Outline each uninfected red blood cell.
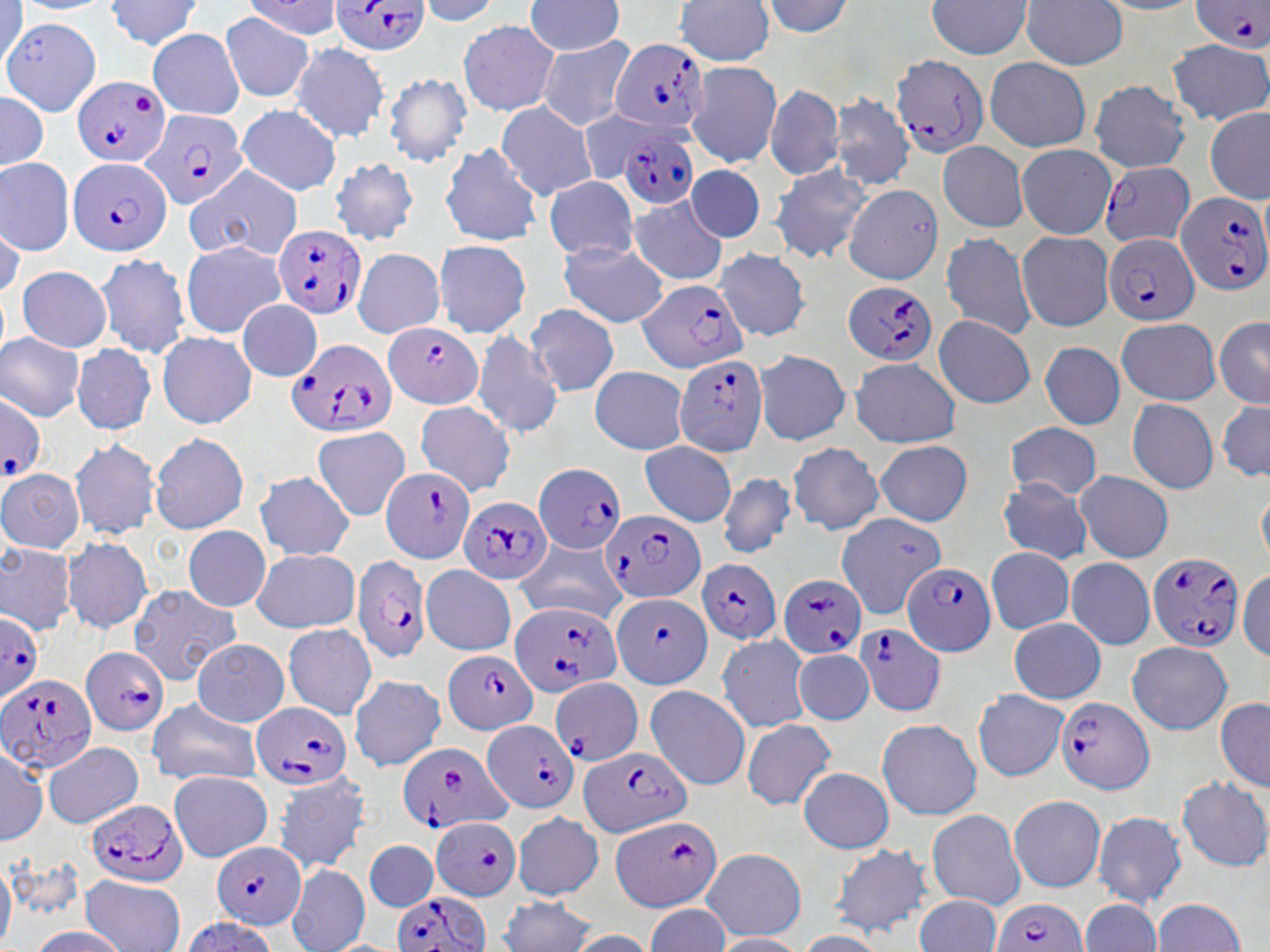
Approximate bounding boxes as [x1, y1, x2, y2] in pixels.
Uninfected red blood cells: [104, 0, 198, 51], [526, 0, 622, 52], [673, 0, 774, 66], [923, 0, 1034, 52], [1011, 0, 1128, 66], [768, 2, 857, 43], [3, 12, 100, 116], [223, 12, 313, 98], [461, 23, 557, 113], [147, 30, 245, 123], [541, 38, 633, 132], [1169, 42, 1270, 122], [289, 45, 389, 144], [986, 58, 1087, 154], [697, 64, 780, 164], [385, 71, 471, 165], [768, 89, 840, 179], [835, 91, 911, 189], [1093, 95, 1189, 169], [985, 96, 1089, 151], [500, 102, 595, 201], [1204, 102, 1268, 206], [238, 106, 340, 196], [685, 129, 774, 166], [444, 144, 539, 245], [937, 145, 1026, 229], [1019, 145, 1109, 240], [1, 156, 72, 256], [333, 163, 419, 245], [773, 163, 868, 263], [688, 168, 761, 240], [546, 178, 634, 256], [845, 181, 943, 287], [185, 183, 301, 261], [629, 197, 727, 284], [1021, 234, 1111, 330], [945, 235, 1034, 337], [561, 240, 670, 327], [185, 244, 283, 335], [439, 244, 527, 336], [722, 249, 811, 339], [99, 252, 188, 359], [355, 252, 441, 336], [21, 268, 110, 352], [242, 301, 318, 378], [527, 306, 617, 396], [1216, 315, 1270, 407], [934, 316, 1032, 407], [1114, 321, 1221, 409], [1, 332, 78, 423], [477, 332, 562, 438], [161, 333, 260, 428], [76, 345, 154, 435], [1040, 345, 1124, 429], [758, 352, 848, 444], [851, 363, 959, 446], [594, 369, 687, 453], [1213, 392, 1270, 485], [1127, 399, 1217, 495], [417, 403, 513, 490], [1010, 423, 1097, 502], [148, 428, 249, 536], [312, 429, 405, 518], [73, 440, 158, 537], [878, 443, 967, 527], [641, 444, 734, 524], [791, 445, 881, 535], [1078, 471, 1173, 560], [255, 473, 356, 560], [0, 475, 86, 554], [1000, 475, 1093, 562], [721, 477, 793, 556], [837, 514, 930, 612], [183, 526, 269, 610], [67, 538, 151, 632], [0, 542, 76, 637], [518, 545, 625, 622], [992, 548, 1071, 634], [249, 551, 357, 631], [1068, 560, 1153, 647], [424, 565, 514, 655], [131, 589, 241, 683], [1010, 620, 1102, 706], [286, 625, 374, 717], [719, 635, 807, 730], [1124, 638, 1232, 735], [194, 641, 288, 727], [798, 652, 873, 724], [354, 677, 441, 772], [648, 686, 750, 788], [975, 689, 1069, 779], [1212, 691, 1268, 789], [150, 704, 262, 786], [745, 719, 834, 812], [878, 719, 980, 817], [4, 737, 46, 852], [45, 744, 142, 831], [797, 766, 893, 854], [170, 775, 270, 861], [1179, 776, 1250, 869], [275, 777, 370, 871], [1009, 792, 1105, 893], [509, 807, 600, 902], [926, 811, 1028, 909], [1096, 815, 1185, 909], [367, 843, 436, 912], [828, 844, 930, 940], [706, 854, 800, 939], [291, 868, 368, 952], [79, 876, 184, 952], [916, 897, 998, 952], [500, 898, 593, 952], [1155, 900, 1245, 952], [1081, 901, 1160, 952].

Summary:
  - Plasmodium falciparum-infected red blood cell locations: [321, 0, 435, 57], [1188, 1, 1270, 52], [611, 38, 708, 133], [891, 50, 989, 162], [72, 74, 170, 167], [142, 112, 248, 211], [622, 136, 697, 207], [1101, 156, 1195, 250], [66, 157, 175, 254], [1173, 194, 1270, 297], [275, 228, 364, 317], [1105, 230, 1199, 325], [837, 279, 942, 365], [639, 285, 745, 376], [381, 321, 484, 410], [287, 338, 393, 436], [672, 348, 771, 456], [1, 398, 41, 479], [536, 466, 623, 552], [383, 471, 473, 563], [460, 499, 552, 585], [602, 515, 705, 599], [1146, 553, 1247, 653], [355, 557, 430, 664], [696, 557, 784, 643], [905, 566, 992, 655], [784, 579, 864, 655], [609, 590, 713, 688], [510, 607, 618, 697], [0, 608, 40, 715], [857, 628, 945, 716], [82, 646, 165, 736], [443, 646, 540, 738], [0, 669, 94, 780], [553, 680, 640, 765], [1054, 696, 1158, 791], [255, 704, 349, 789], [481, 714, 580, 814], [396, 734, 508, 833], [580, 744, 690, 838], [83, 799, 191, 885], [608, 814, 717, 910], [426, 815, 528, 899], [215, 841, 306, 928], [392, 891, 493, 952], [995, 900, 1085, 952]
  - Slide-level diagnosis: Plasmodium falciparum
  - Modality: optical microscopy
  - Magnification: 1000x
  - Stain: May-Grünwald-Giemsa
  - Image size: 1270×952 pixels
  - Preparation: thin blood film
  - Field of view: single